Locate the cells, classifying each as a parasitized RBC, an uninfected RBC, or a WBC.
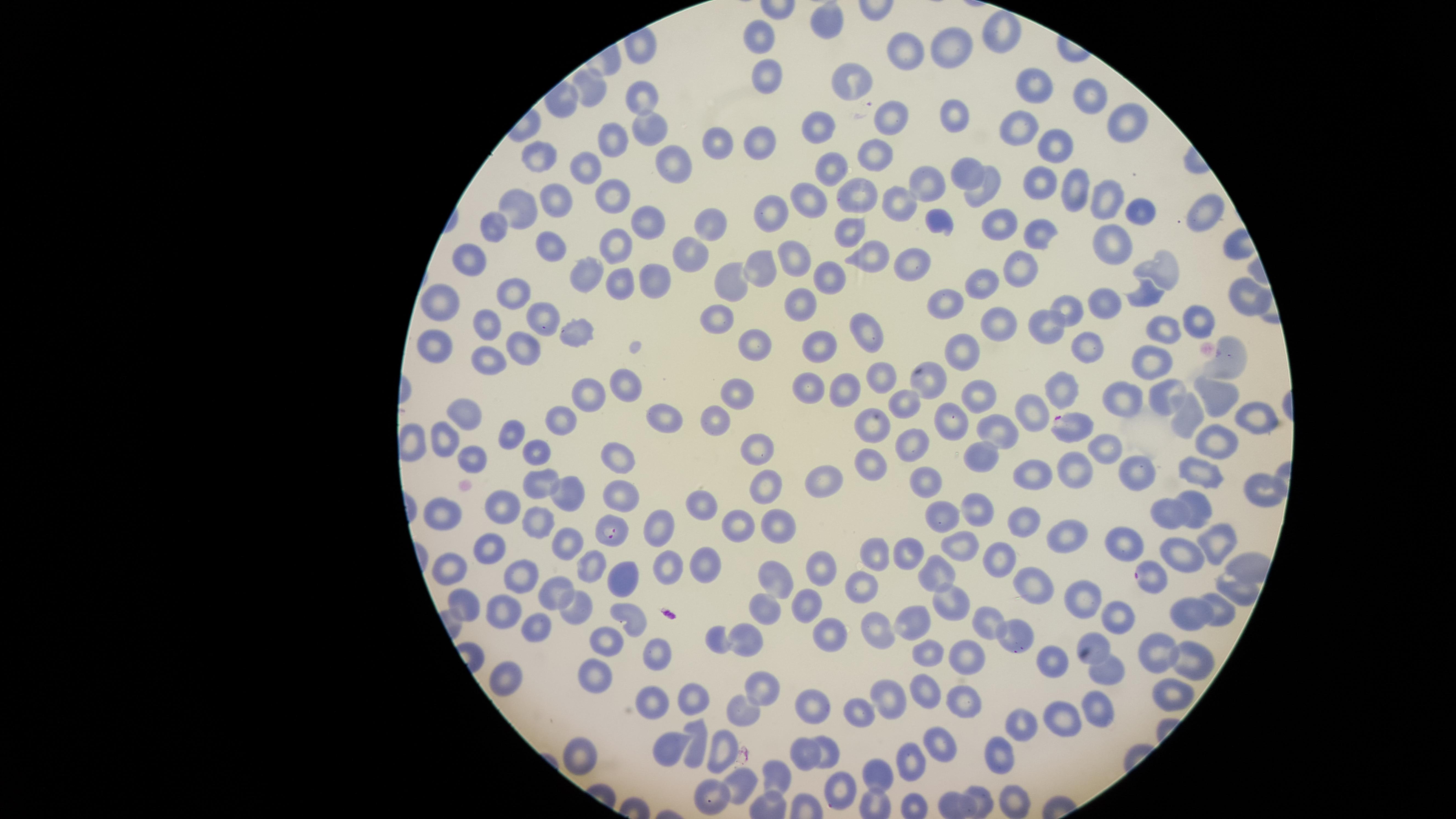
Approximate marker points as (x, y) in pixels.
Parasitized RBCs: (1071, 427), (612, 530), (1146, 573), (1015, 638), (839, 791).
Uninfected RBCs: (828, 21), (995, 37), (763, 40), (953, 50), (906, 55), (770, 74), (845, 80), (591, 89), (1036, 90), (644, 94), (1086, 96), (956, 116), (892, 120), (817, 122), (1124, 123), (1026, 128), (648, 129), (605, 136), (765, 138), (1054, 141), (718, 146), (872, 156), (538, 157), (677, 160), (832, 165), (582, 166), (964, 171), (925, 179), (1068, 184), (1045, 189), (984, 190), (615, 195), (1108, 195), (857, 197), (549, 199), (811, 200), (904, 203), (518, 208), (771, 208), (1134, 211), (1203, 215), (938, 219), (648, 220), (708, 220), (1003, 220), (493, 227), (852, 229), (1043, 231), (548, 242), (1116, 243), (616, 249), (685, 249), (790, 258), (869, 258), (470, 263), (914, 263), (1159, 267), (585, 270), (761, 271), (1024, 273), (829, 274), (656, 276), (615, 278), (725, 280), (979, 280), (518, 289), (1242, 294), (440, 296), (1148, 299), (946, 301), (804, 304), (1107, 309), (1072, 314), (1188, 315), (544, 318), (716, 319), (998, 324), (1160, 325), (1042, 326), (484, 327), (574, 330), (865, 337), (1089, 342), (436, 343), (525, 344), (816, 344), (755, 345), (960, 351), (1234, 359), (483, 360), (1141, 366), (877, 378), (929, 383), (1221, 384), (1058, 387), (810, 389), (628, 390), (738, 390), (588, 392), (845, 393), (980, 396), (1120, 398), (1164, 399), (901, 404), (1246, 410), (465, 412), (665, 415), (714, 417), (1036, 417), (554, 418), (1188, 420), (949, 423), (870, 425), (512, 432), (1002, 435), (444, 438), (1218, 439), (910, 442), (1103, 443), (762, 447), (537, 449), (983, 456), (617, 457), (870, 460), (1068, 464), (1028, 466), (1199, 469), (1135, 472), (927, 475), (826, 482), (542, 484), (1263, 484), (569, 490), (761, 490), (619, 497), (698, 500), (969, 502), (1197, 507), (503, 508), (1171, 510), (449, 512), (1019, 518), (734, 519), (943, 519), (538, 521), (772, 528), (663, 530), (1067, 533), (1125, 535), (1220, 538), (566, 541), (962, 544), (489, 548), (875, 549), (907, 553), (1184, 554), (998, 558), (819, 559), (699, 563), (595, 564), (456, 566), (768, 568), (665, 571), (623, 575), (937, 575), (524, 576), (1233, 582), (1035, 585), (860, 588), (555, 591), (1080, 596), (950, 599), (770, 600), (462, 602), (1218, 606), (570, 607), (499, 608), (800, 610), (1188, 614), (631, 615), (1117, 615), (536, 621), (989, 621), (869, 627), (908, 630), (829, 632), (750, 634), (1096, 637), (714, 639), (607, 642), (1156, 648), (662, 649), (1190, 655), (930, 657), (968, 657), (1055, 658), (1104, 672), (593, 674), (508, 679), (761, 684), (925, 687), (1166, 695), (690, 699), (809, 702), (964, 702), (651, 703), (858, 703), (884, 705), (1093, 706), (738, 709), (1067, 714), (1026, 719), (670, 743), (824, 744), (940, 744), (699, 747), (1003, 751), (575, 752), (722, 755), (802, 755), (905, 762), (877, 774), (779, 777), (744, 782), (709, 795), (1014, 798), (976, 800), (947, 803).
No WBCs identified.

capture = smartphone photograph through the microscope eyepiece
image size = 1456×819 pixels
preparation = thin blood film
visible region = circular
field of view = single
stain = Giemsa
species = Plasmodium falciparum